Give the extent of all Plasmodium ovale-infected red blood cells.
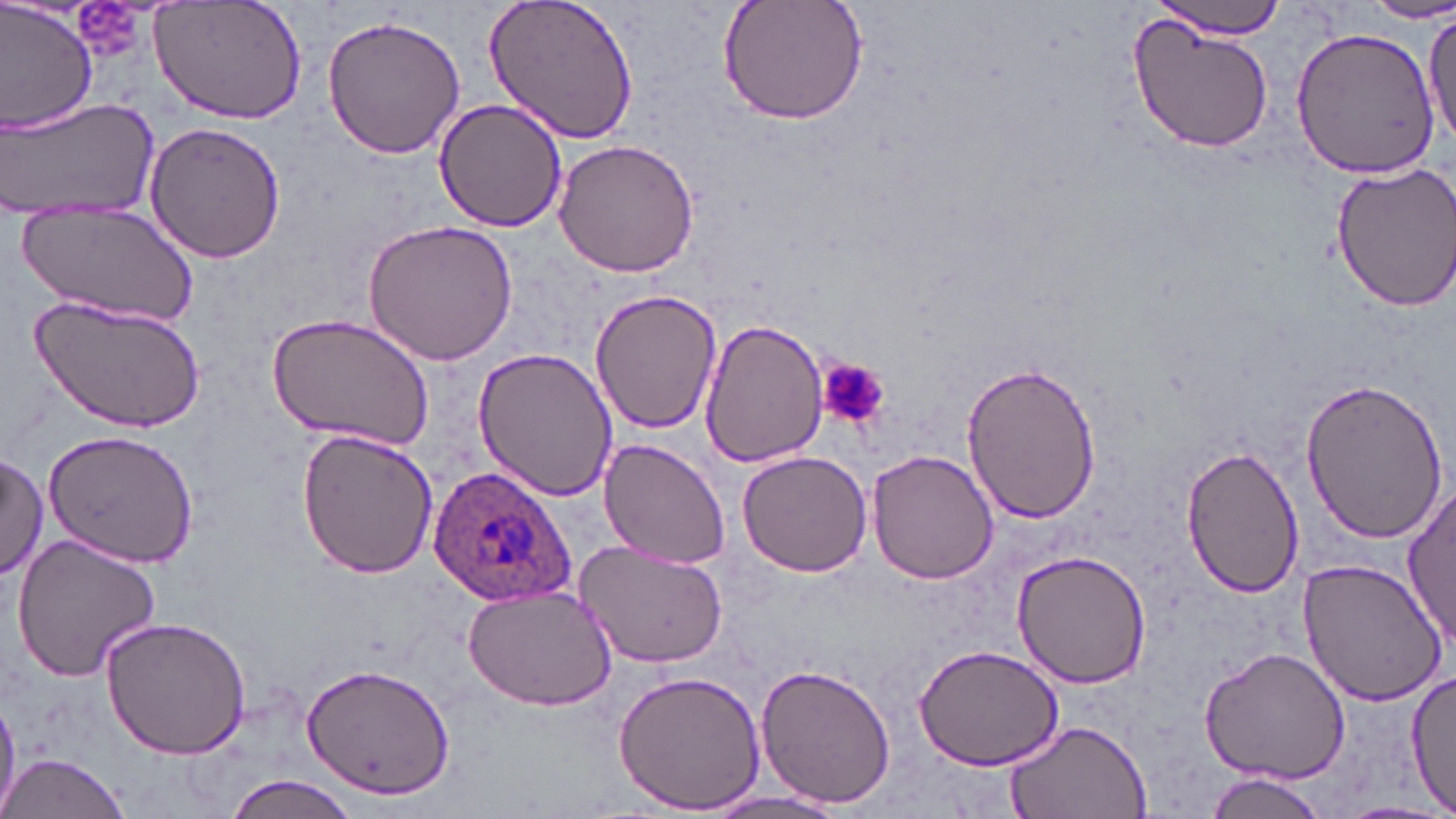

Approximate bounding boxes as named x1/y1/x2/y2 corners in pixels.
Plasmodium ovale-infected red blood cells: (x1=420, y1=464, x2=582, y2=606).

Uninfected red blood cell locations: (x1=0, y1=0, x2=98, y2=135), (x1=148, y1=0, x2=306, y2=127), (x1=483, y1=0, x2=642, y2=145), (x1=718, y1=0, x2=870, y2=127), (x1=1149, y1=0, x2=1294, y2=39), (x1=1362, y1=3, x2=1456, y2=25), (x1=1424, y1=10, x2=1456, y2=155), (x1=320, y1=13, x2=467, y2=162), (x1=1128, y1=18, x2=1275, y2=156), (x1=1289, y1=24, x2=1442, y2=180), (x1=1, y1=95, x2=158, y2=220), (x1=432, y1=98, x2=569, y2=233), (x1=144, y1=122, x2=285, y2=264), (x1=553, y1=141, x2=700, y2=278), (x1=1327, y1=157, x2=1456, y2=314), (x1=18, y1=205, x2=200, y2=327), (x1=362, y1=218, x2=521, y2=368), (x1=33, y1=289, x2=206, y2=433), (x1=591, y1=289, x2=721, y2=438), (x1=265, y1=312, x2=436, y2=452), (x1=700, y1=319, x2=827, y2=471), (x1=473, y1=347, x2=619, y2=501), (x1=960, y1=356, x2=1100, y2=525), (x1=1298, y1=376, x2=1451, y2=543), (x1=41, y1=427, x2=201, y2=566), (x1=297, y1=429, x2=439, y2=580), (x1=598, y1=439, x2=733, y2=571), (x1=1180, y1=444, x2=1305, y2=600), (x1=736, y1=448, x2=876, y2=577), (x1=0, y1=449, x2=47, y2=583), (x1=866, y1=449, x2=1000, y2=585), (x1=1403, y1=484, x2=1455, y2=653), (x1=10, y1=533, x2=162, y2=681), (x1=575, y1=542, x2=728, y2=669), (x1=1013, y1=549, x2=1154, y2=689), (x1=1297, y1=557, x2=1449, y2=709), (x1=462, y1=585, x2=615, y2=713), (x1=100, y1=617, x2=254, y2=760), (x1=913, y1=642, x2=1066, y2=772), (x1=1199, y1=646, x2=1351, y2=784), (x1=299, y1=661, x2=456, y2=800), (x1=755, y1=663, x2=896, y2=810), (x1=1405, y1=669, x2=1456, y2=812), (x1=611, y1=671, x2=767, y2=815), (x1=0, y1=695, x2=19, y2=817), (x1=1003, y1=718, x2=1154, y2=819), (x1=1, y1=751, x2=133, y2=819), (x1=1202, y1=771, x2=1332, y2=818), (x1=224, y1=776, x2=362, y2=819), (x1=701, y1=788, x2=849, y2=817), (x1=1332, y1=800, x2=1456, y2=819). Platelet locations: (x1=817, y1=357, x2=888, y2=427). Slide-level diagnosis: Plasmodium ovale. May-Grünwald-Giemsa stain. Captured at 1000x magnification. Optical microscopy. Image is 1456×819 pixels. One field of a larger specimen. Thin blood smear.